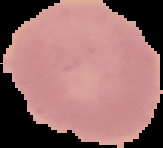

malaria status = uninfected
preparation = thin blood film
image type = segmented cell region with the area outside set to black
image size = 163×148 pixels